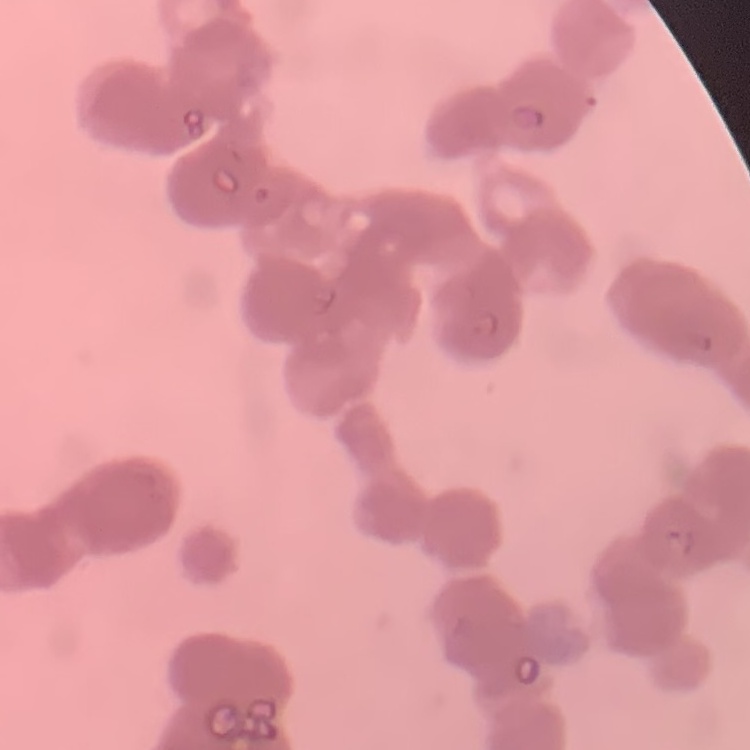

Summary:
  - Red blood cell morphology: rouleaux formation
  - Preparation: thin blood film
  - Stain: Field's or Giemsa
  - Image type: one tile cut from a larger photomicrograph